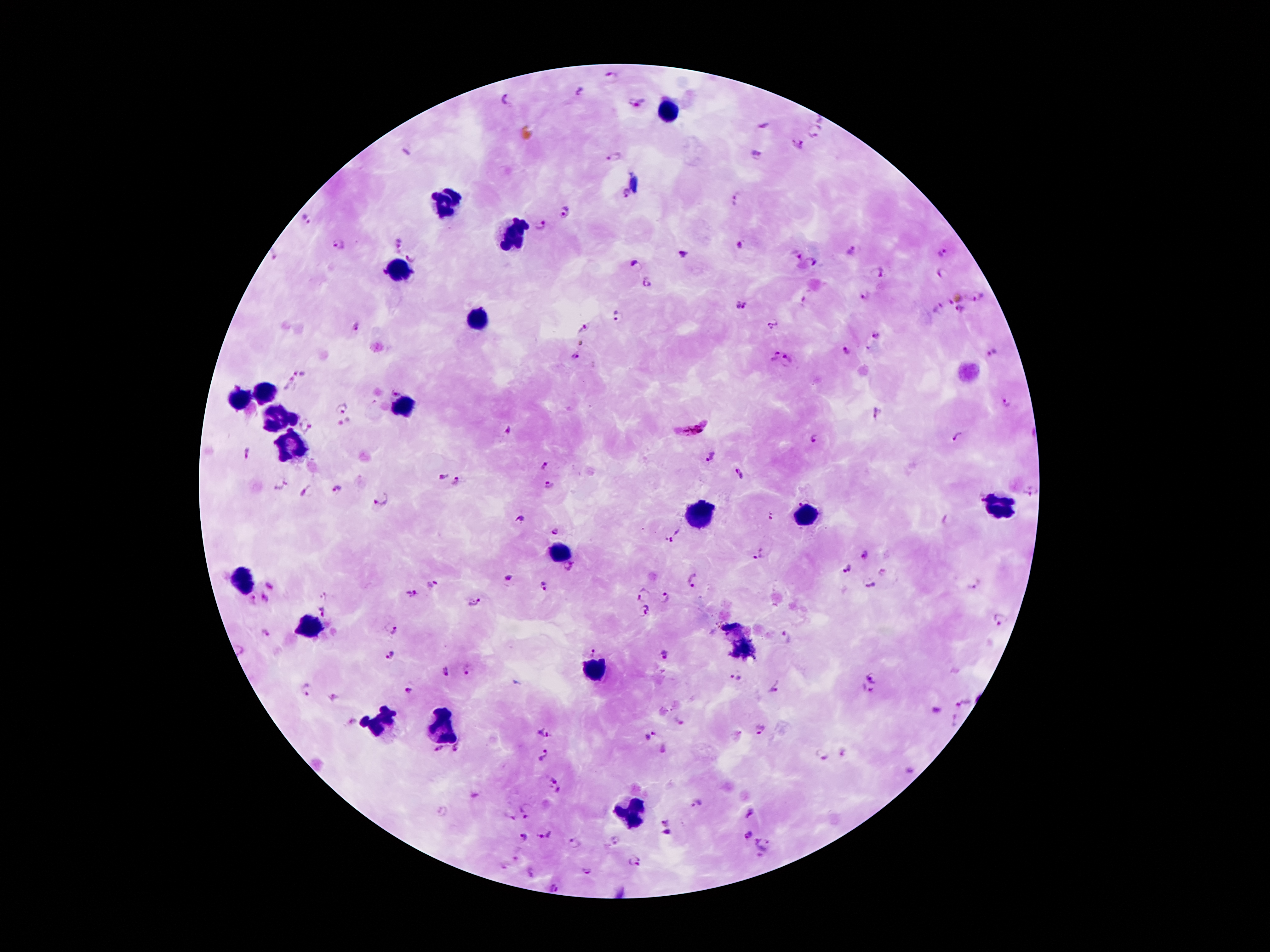
Approximate centers as [x, y] in pixels.
Summary:
  - Leukocyte locations: [671, 107], [446, 202], [514, 234], [400, 271], [478, 318], [264, 393], [239, 401], [400, 407], [274, 419], [289, 452], [1000, 505], [803, 515], [694, 517], [558, 554], [243, 577], [310, 625], [740, 648], [593, 673], [379, 724], [442, 726], [629, 812]
  - Plasmodium parasite locations: [612, 78], [580, 92], [507, 99], [637, 102], [819, 119], [816, 131], [798, 145], [616, 157], [754, 157], [626, 195], [736, 196], [565, 212], [306, 218], [542, 226], [398, 243], [340, 245], [741, 245], [852, 251], [943, 253], [273, 254], [684, 254], [797, 255], [411, 258], [813, 263], [635, 265], [878, 273], [382, 274], [943, 274], [647, 282], [866, 296], [979, 298], [807, 302], [733, 304], [747, 307], [937, 309], [962, 310], [618, 316], [775, 324], [357, 325], [584, 328], [875, 335], [581, 342], [845, 352], [993, 353], [775, 356], [575, 357], [789, 361], [299, 372], [290, 382], [1006, 403], [341, 408], [877, 414], [307, 426], [691, 428], [507, 429], [957, 437], [814, 439], [247, 453], [711, 456], [544, 465], [740, 474], [442, 476], [457, 483], [278, 484], [548, 485], [337, 489], [307, 490], [1031, 491], [803, 498], [382, 499], [769, 516], [518, 519], [949, 521], [558, 530], [673, 536], [759, 555], [864, 557], [569, 566], [845, 570], [509, 577], [693, 580], [269, 584], [972, 584], [544, 585], [432, 586], [868, 586], [411, 593], [643, 594], [324, 595], [264, 598], [251, 600], [666, 600], [475, 601], [323, 610], [646, 613], [1000, 620], [392, 628], [265, 634], [788, 637], [593, 652], [391, 655], [664, 655], [468, 669], [446, 672], [735, 677], [873, 678], [306, 691], [408, 691], [772, 691], [864, 693], [333, 698], [965, 704], [679, 720], [956, 720], [351, 722], [761, 730], [545, 733], [651, 737], [458, 748], [439, 750], [845, 753], [545, 756], [822, 756], [552, 779], [560, 791], [697, 804], [442, 812], [524, 812], [750, 813], [510, 818], [664, 822], [667, 834], [544, 835], [747, 835], [523, 837], [613, 840], [572, 844], [765, 845], [518, 853], [635, 860], [504, 867], [586, 871], [530, 873], [555, 887]
  - Field of view: one from this slide
  - Capture: smartphone camera through the microscope eyepiece
  - Magnification: 100x
  - Stain: Giemsa
  - Preparation: thick blood film
  - Image size: 1270×952 pixels
  - Patient malaria status: infected with Plasmodium falciparum